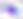
modality = photomicrograph
magnification = 400x
identification = Toxoplasma gondii